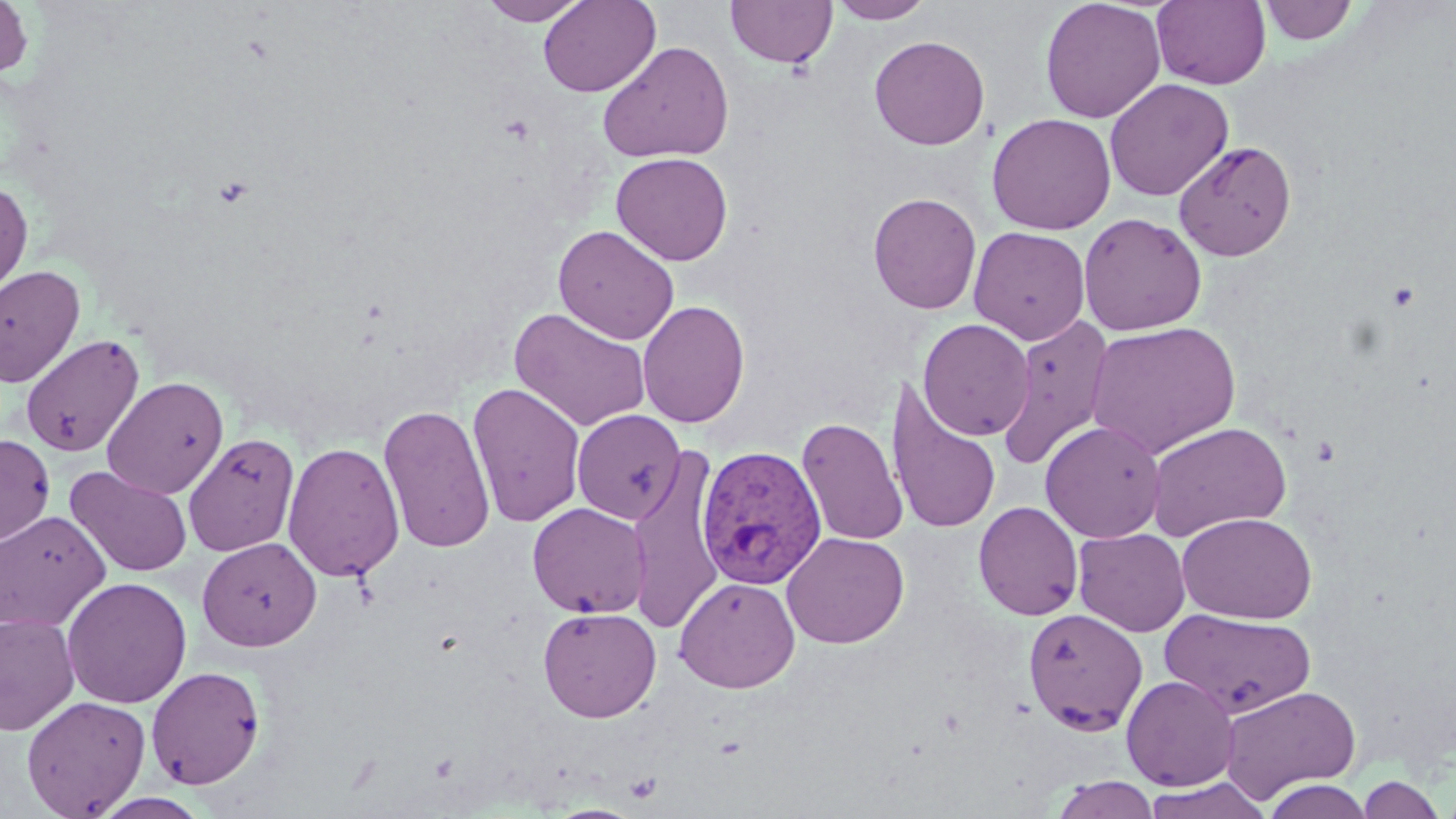
slide-level diagnosis = Plasmodium vivax
platelet locations = approximate bounding boxes as (x1,y1)-(x2,y2) corner pairs in pixels: (1386,281)-(1421,311), (1310,435)-(1341,467)
stain = May-Grünwald-Giemsa
magnification = 1000x
modality = light microscopy
field of view = single
Plasmodium vivax-infected red blood cell locations = approximate bounding boxes as (x1,y1)-(x2,y2) corner pairs in pixels: (695,445)-(828,589)
image size = 1456×819 pixels
preparation = thin blood film
uninfected red blood cell locations = approximate bounding boxes as (x1,y1)-(x2,y2) corner pairs in pixels: (0,0)-(34,79), (478,0)-(590,25), (538,0)-(660,97), (1039,0)-(1166,123), (1258,0)-(1359,45), (725,1)-(837,69), (827,1)-(935,24), (1152,1)-(1271,89), (869,35)-(990,150), (597,40)-(734,163), (1104,78)-(1233,201), (987,113)-(1116,234), (1173,141)-(1297,261), (611,152)-(733,265), (0,181)-(33,302), (867,192)-(982,314), (1078,213)-(1208,336), (553,225)-(680,344), (968,226)-(1090,345), (928,247)-(1087,409), (0,265)-(85,388), (637,299)-(750,428), (509,307)-(652,431), (996,314)-(1116,472), (918,318)-(1035,440), (1085,322)-(1241,458), (20,334)-(145,457), (102,376)-(229,499), (885,378)-(1001,536), (467,381)-(587,528), (378,403)-(496,553), (571,409)-(685,524), (796,416)-(908,545), (1040,421)-(1166,543), (1147,421)-(1292,541), (0,433)-(55,545), (183,433)-(300,556), (282,441)-(405,583), (624,446)-(727,633), (65,465)-(192,577), (973,501)-(1084,620), (527,502)-(652,618), (0,509)-(111,633), (1176,512)-(1318,624), (1073,528)-(1191,637), (781,532)-(909,649), (196,537)-(322,651), (674,576)-(800,693), (61,577)-(192,709), (537,607)-(662,722), (1022,607)-(1148,735), (1161,608)-(1315,718), (0,612)-(80,735), (145,665)-(266,789), (1121,674)-(1240,791), (1220,685)-(1360,802), (21,695)-(151,818), (1355,774)-(1449,818), (1047,775)-(1163,818), (1140,777)-(1272,819), (1259,778)-(1376,818)